Classify this cell by malaria status.
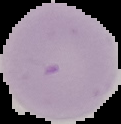
It is uninfected.

Cell region segmented out of the field of view; the surrounding area is masked to black. Image is 121×124 pixels. From a thin blood smear.